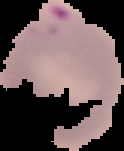
image type = segmented cell region on a black background
preparation = thin blood film
malaria status = parasitized
image size = 124×151 pixels